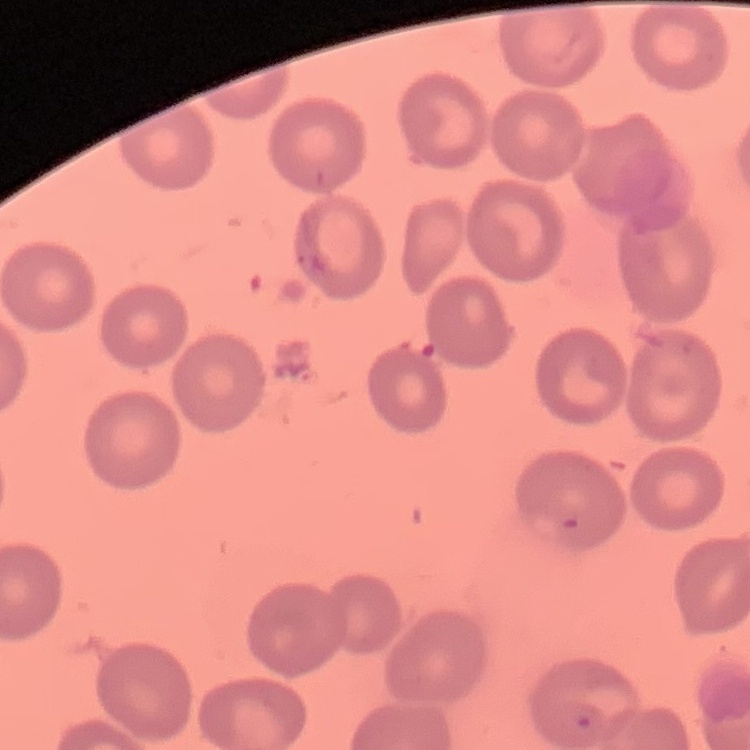
red blood cell morphology = no rouleaux formation
image type = square crop of a larger photomicrograph
stain = Field's or Giemsa
preparation = thin peripheral smear